Report the malaria status of this cell.
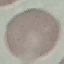
It is uninfected.

Summary:
  - Stain: Giemsa
  - Capture: smartphone through the microscope eyepiece
  - Image type: automatically extracted cell patch, resized to 64 × 64 pixels
  - Preparation: thin blood smear